Comment on the morphology of the erythrocytes.
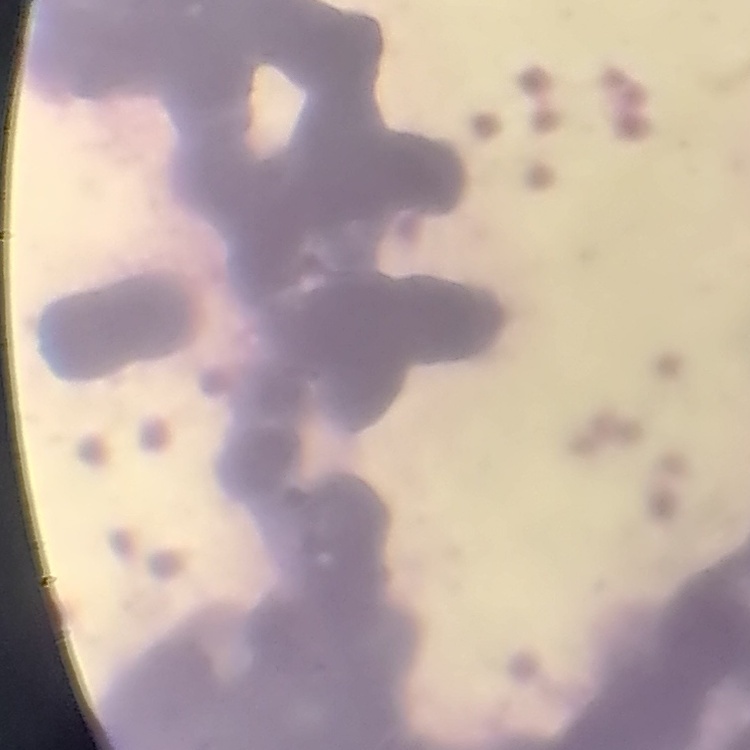
Rouleaux formation.

Summary:
  - Stain: Field's or Giemsa
  - Image type: one tile cut from a larger photomicrograph
  - Preparation: thin blood smear